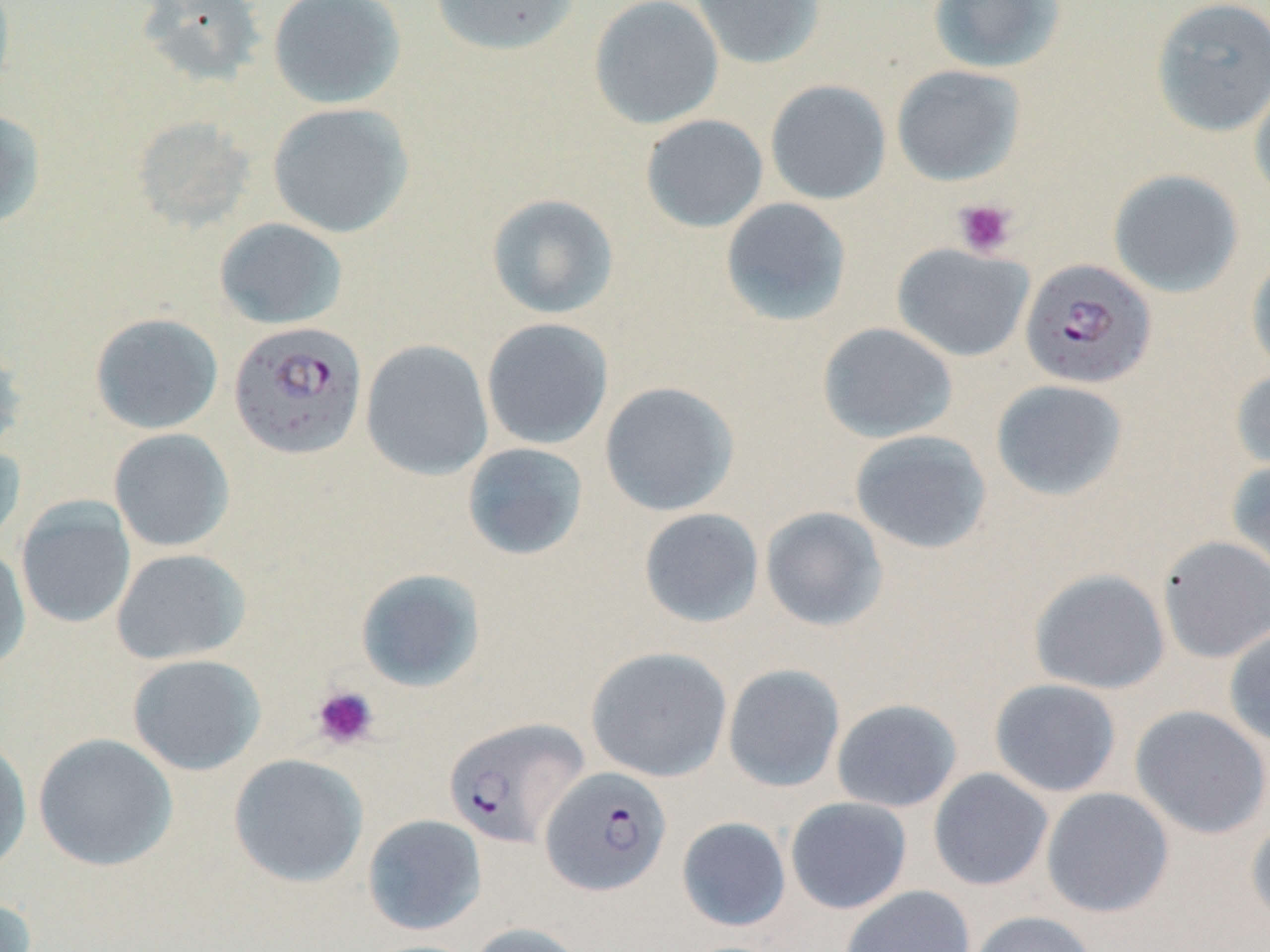

{
  "slide_level_diagnosis": "Plasmodium falciparum",
  "image_size": "1270×952 pixels",
  "field_of_view": "single",
  "uninfected_red_blood_cell_locations": "approximate bounding boxes as [x1, y1, x2, y2] in pixels: [267, 0, 407, 109], [429, 0, 580, 57], [589, 0, 724, 130], [690, 0, 826, 69], [927, 0, 1067, 74], [1150, 0, 1270, 136], [135, 1, 267, 88], [891, 64, 1026, 186], [1250, 76, 1270, 206], [765, 80, 891, 204], [267, 102, 414, 238], [0, 108, 47, 229], [640, 114, 769, 233], [131, 115, 256, 232], [1108, 169, 1244, 298], [486, 193, 619, 319], [720, 197, 852, 326], [215, 218, 348, 330], [892, 243, 1034, 362], [1246, 252, 1270, 377], [89, 312, 223, 434], [481, 317, 614, 450], [817, 322, 958, 443], [360, 339, 493, 480], [0, 340, 28, 458], [1231, 368, 1270, 475], [990, 379, 1129, 502], [599, 381, 740, 516], [108, 428, 235, 552], [849, 430, 992, 555], [0, 441, 26, 549], [461, 442, 589, 561], [1227, 459, 1270, 584], [16, 497, 136, 629], [760, 506, 889, 632], [638, 508, 764, 628], [1157, 535, 1270, 663], [0, 545, 31, 671], [111, 548, 251, 665], [355, 567, 486, 692], [1029, 568, 1171, 694], [1224, 624, 1270, 748], [585, 646, 733, 782], [127, 653, 266, 776], [722, 663, 845, 792], [989, 678, 1122, 797], [831, 698, 962, 812], [1130, 705, 1270, 839], [33, 733, 178, 871], [0, 735, 32, 876], [228, 753, 369, 887], [928, 768, 1053, 891], [1041, 787, 1175, 918], [785, 797, 913, 914], [362, 814, 487, 936], [1246, 815, 1270, 930], [676, 816, 792, 932], [840, 885, 976, 952], [0, 893, 38, 952], [968, 910, 1098, 952], [466, 922, 588, 952]",
  "preparation": "thin blood film",
  "stain": "May-Grünwald-Giemsa",
  "plasmodium_falciparum_infected_red_blood_cell_locations": "approximate bounding boxes as [x1, y1, x2, y2] in pixels: [1019, 258, 1156, 390], [227, 321, 368, 461], [443, 716, 588, 849], [540, 766, 672, 896]",
  "magnification": "1000x",
  "platelet_locations": "approximate bounding boxes as [x1, y1, x2, y2] in pixels: [953, 198, 1018, 258], [311, 685, 378, 749]",
  "modality": "light microscopy"
}